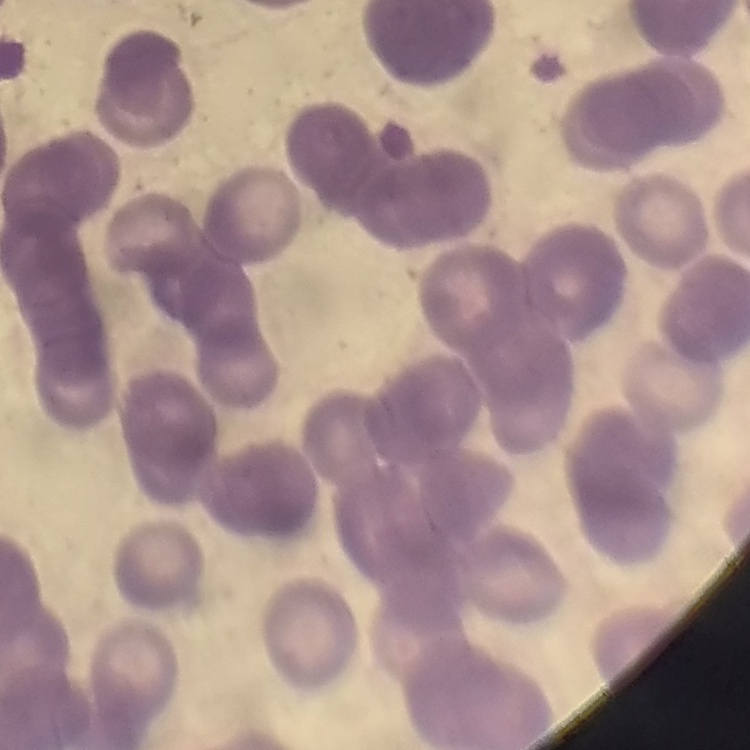
Summary:
  - Red blood cell morphology: rouleaux formation
  - Preparation: thin blood smear
  - Image type: square crop of a larger photomicrograph
  - Stain: Field's or Giemsa